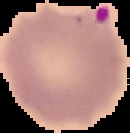
preparation: thin blood smear
image_size: 130×133 pixels
image_type: segmented cell region on a black background
malaria_status: parasitized